State which parasite is depicted.
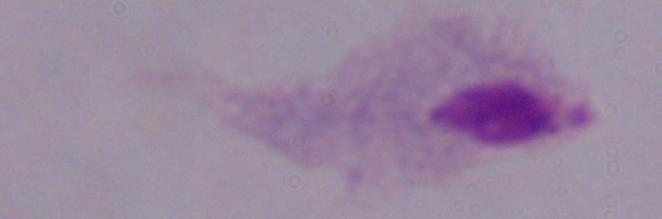

A trichomonad.

1000x magnification. Micrograph.